Outline each blood parasite and name the species.
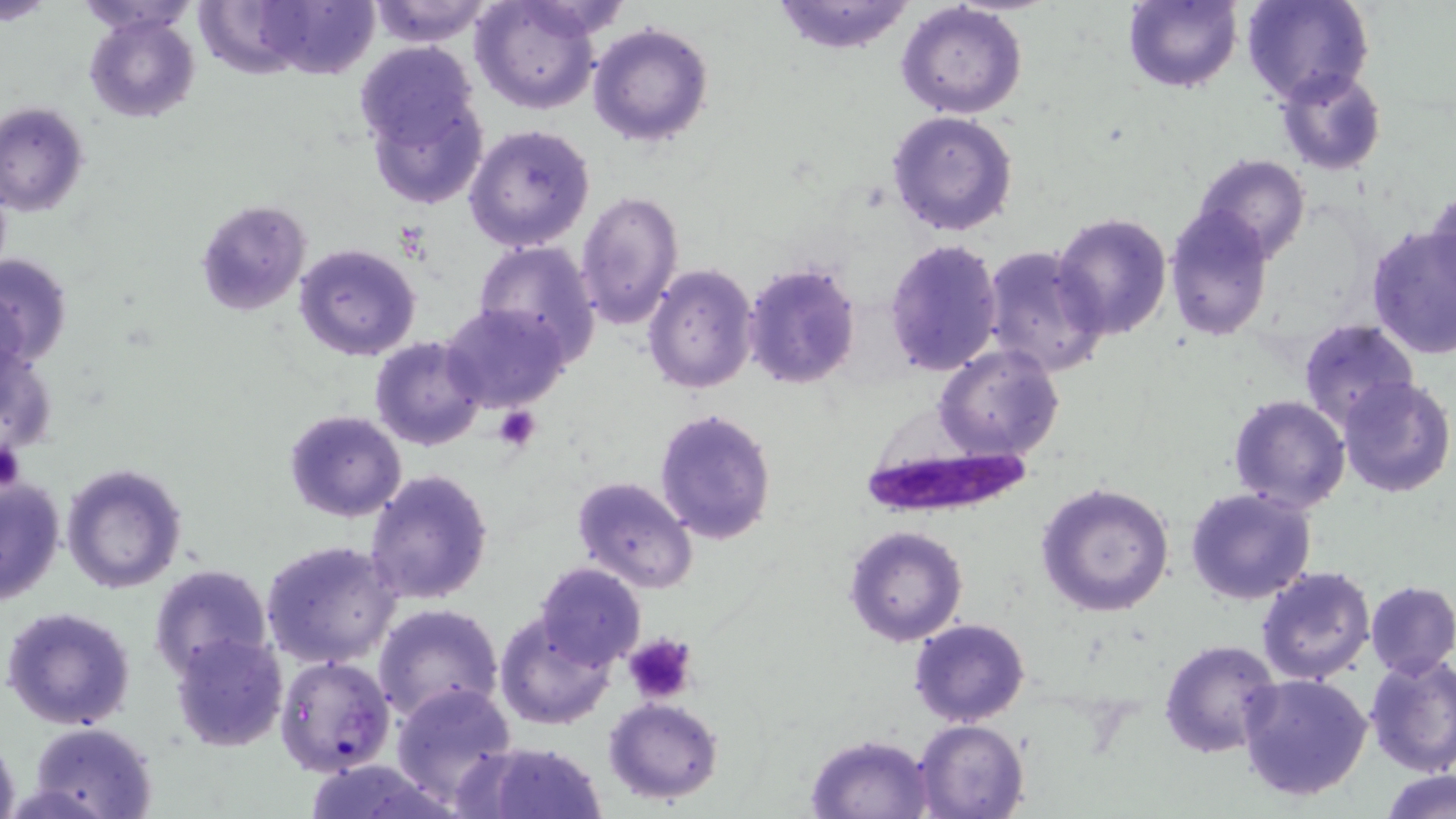
Approximate bounding boxes as (x1, y1, x2, y2) in pixels.
Plasmodium falciparum-infected red blood cells: (850, 426, 1031, 532), (275, 654, 396, 775).
No Plasmodium ovale, Plasmodium malariae, Plasmodium vivax, Babesia divergens, or Trypanosoma brucei observed.

slide-level diagnosis = Plasmodium falciparum
uninfected red blood cell locations = approximate bounding boxes as (x1, y1, x2, y2) in pixels: (0, 0, 53, 23), (74, 0, 199, 34), (365, 0, 497, 46), (769, 0, 918, 54), (1121, 0, 1242, 92), (1242, 0, 1372, 108), (470, 1, 601, 113), (231, 2, 377, 79), (896, 2, 1027, 118), (84, 13, 199, 123), (588, 22, 715, 148), (352, 40, 482, 163), (1275, 68, 1387, 175), (360, 80, 489, 210), (0, 101, 90, 216), (887, 109, 1019, 237), (463, 124, 596, 252), (1189, 154, 1311, 265), (1426, 187, 1456, 291), (575, 189, 684, 329), (193, 199, 311, 318), (1164, 205, 1275, 341), (1051, 212, 1175, 341), (1365, 224, 1456, 358), (883, 239, 1002, 377), (471, 240, 602, 360), (293, 243, 423, 363), (981, 245, 1107, 377), (0, 251, 74, 370), (742, 260, 862, 391), (642, 264, 758, 394), (441, 302, 569, 413), (1298, 319, 1420, 431), (369, 337, 488, 453), (935, 344, 1063, 461), (1337, 376, 1454, 497), (1226, 394, 1350, 514), (284, 409, 407, 523), (654, 409, 777, 545), (60, 460, 187, 594), (363, 468, 494, 606), (571, 475, 699, 593), (0, 477, 66, 605), (1035, 481, 1175, 617), (1185, 487, 1316, 604), (842, 524, 968, 647), (261, 539, 404, 669), (534, 562, 645, 668), (149, 563, 274, 682), (1256, 565, 1377, 683), (1364, 581, 1456, 677), (372, 602, 503, 723), (3, 605, 136, 732), (494, 612, 617, 731), (908, 618, 1032, 728), (170, 632, 288, 751), (1158, 638, 1281, 757), (1363, 653, 1456, 775), (1237, 672, 1372, 802), (389, 682, 516, 805), (601, 697, 725, 803), (914, 719, 1029, 819), (29, 720, 159, 819), (805, 733, 935, 818), (0, 734, 20, 819), (474, 741, 608, 818), (301, 759, 454, 819), (1382, 769, 1455, 819)
image size = 1456×819 pixels
magnification = 1000x
platelet locations = approximate bounding boxes as (x1, y1, x2, y2) in pixels: (493, 406, 542, 451), (0, 438, 25, 492), (621, 634, 700, 706)
preparation = thin blood smear
stain = May-Grünwald-Giemsa
modality = light microscopy
field of view = single